Name the parasite shown.
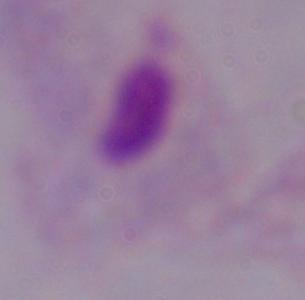

A trichomonad.

Photomicrograph. 1000x magnification.